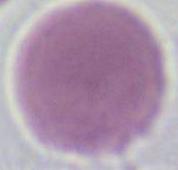

identification: red blood cell
modality: photomicrograph
magnification: 1000x